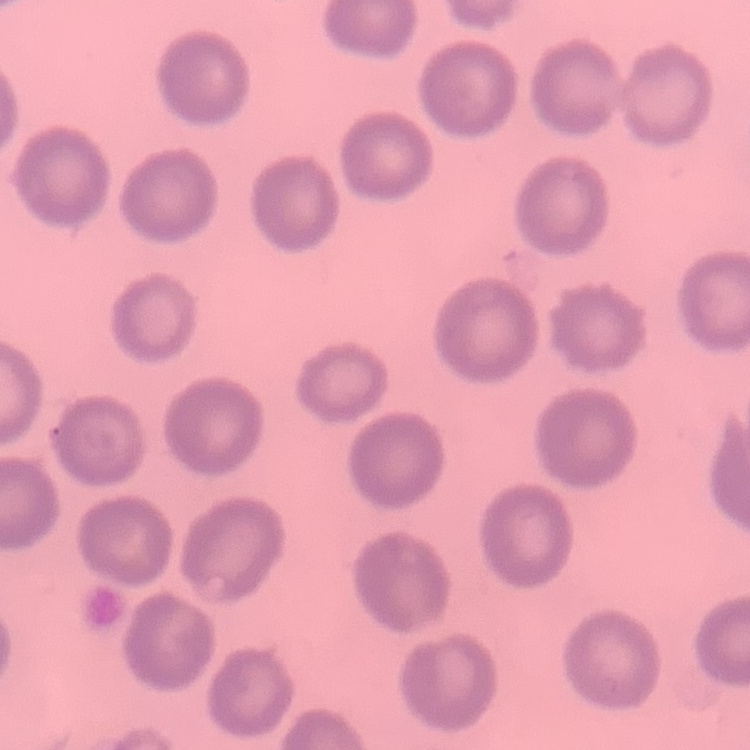
erythrocyte morphology = no rouleaux formation
stain = Field's or Giemsa
image type = square crop of a larger photomicrograph
preparation = thin blood film